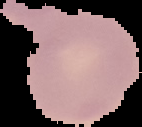

Malaria status: uninfected. Segmented cell region on a black background. Image is 142×127 pixels. From a thin blood smear.